Assess this cell for malaria.
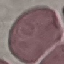

It is uninfected.

Summary:
  - Image type: cell patch, automatically extracted from a larger field of view and resized to 64 × 64 pixels
  - Capture: smartphone through the microscope eyepiece
  - Preparation: thin blood smear
  - Stain: Giemsa